Report the malaria status of this cell.
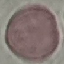

Uninfected.

Summary:
  - Preparation: thin blood film
  - Capture: smartphone camera at the microscope eyepiece
  - Stain: Giemsa
  - Image type: automatically extracted cell patch, resized to 64 × 64 pixels